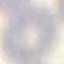
Summary:
  - Malaria status: uninfected
  - Preparation: thin blood film
  - Image type: cell patch, automatically extracted from a larger field of view and resized to 64 × 64 pixels
  - Stain: Giemsa
  - Capture: smartphone camera at the microscope eyepiece